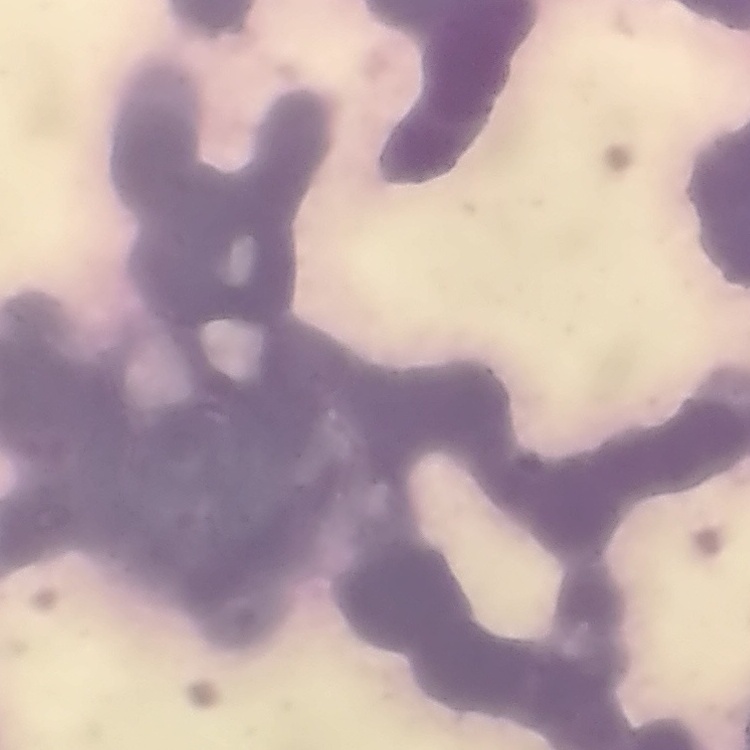
erythrocyte morphology = rouleaux formation
preparation = thin blood film
image type = square crop of a larger photomicrograph
stain = Field's or Giemsa